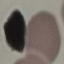
Summary:
  - Result: no malaria parasites seen
  - Capture: smartphone camera at the microscope eyepiece
  - Preparation: thin blood film
  - Image type: automatically extracted cell patch, resized to 64 × 64 pixels
  - Stain: Giemsa